Classify this cell by malaria status.
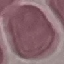
Uninfected.

Photographed with a smartphone camera at the microscope eyepiece. Giemsa stain. Thin smear of blood. Automatically extracted cell patch, resized to 64 × 64 pixels.